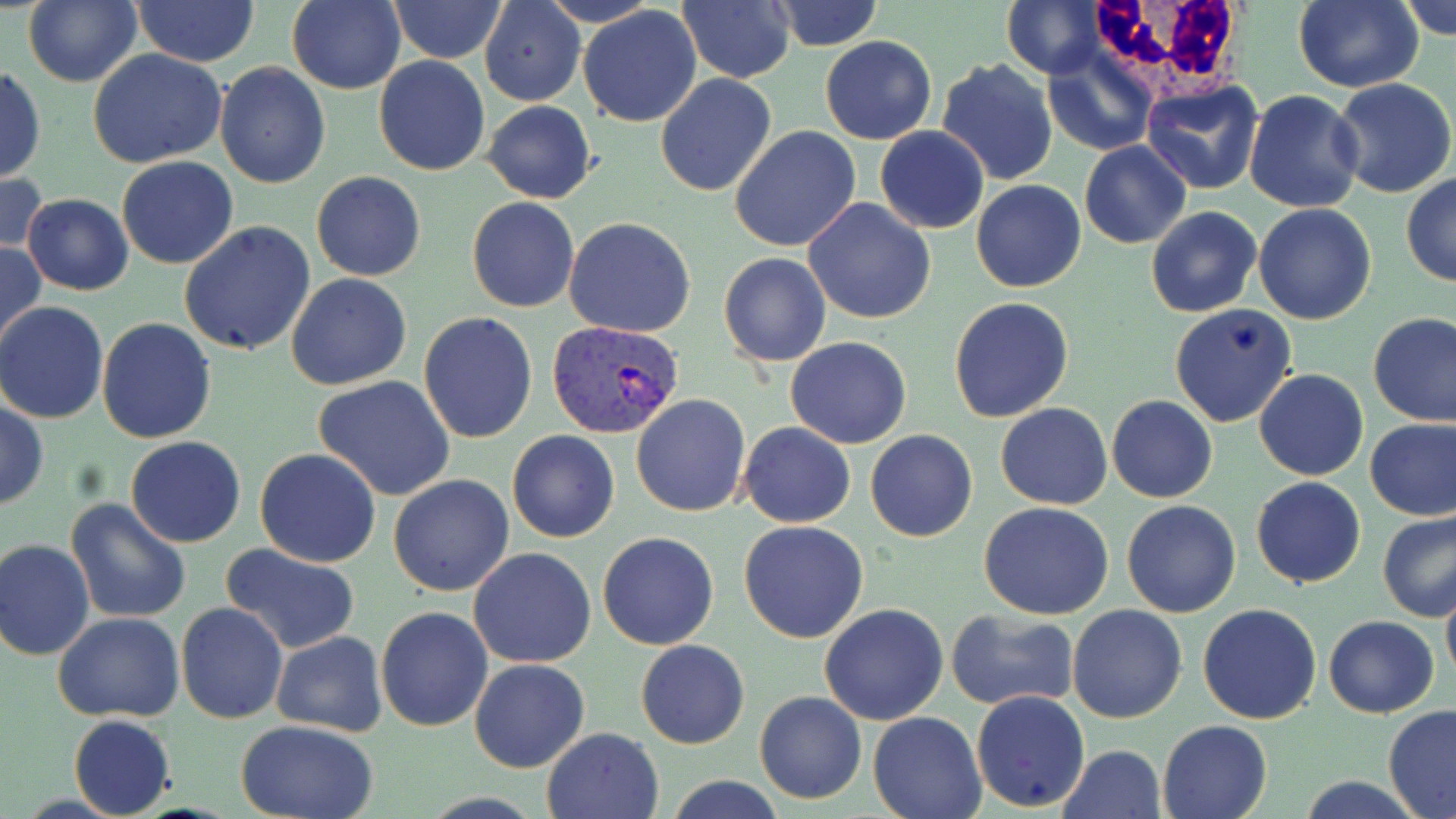
{
  "slide_level_diagnosis": "Plasmodium vivax",
  "field_of_view": "single",
  "white_blood_cell_locations": "approximate bounding boxes as named x1/y1/x2/y2 corners in pixels: (x1=1089, y1=0, x2=1248, y2=102)",
  "modality": "light microscopy",
  "plasmodium_vivax_infected_red_blood_cell_locations": "approximate bounding boxes as named x1/y1/x2/y2 corners in pixels: (x1=547, y1=320, x2=684, y2=439)",
  "stain": "May-Grünwald-Giemsa",
  "uninfected_red_blood_cell_locations": "approximate bounding boxes as named x1/y1/x2/y2 corners in pixels: (x1=23, y1=0, x2=142, y2=88), (x1=285, y1=0, x2=406, y2=93), (x1=537, y1=0, x2=661, y2=27), (x1=767, y1=0, x2=886, y2=51), (x1=1002, y1=0, x2=1105, y2=77), (x1=1293, y1=0, x2=1422, y2=93), (x1=1400, y1=0, x2=1456, y2=39), (x1=132, y1=1, x2=261, y2=67), (x1=390, y1=1, x2=506, y2=64), (x1=678, y1=1, x2=794, y2=83), (x1=480, y1=2, x2=584, y2=107), (x1=578, y1=5, x2=703, y2=129), (x1=820, y1=35, x2=936, y2=145), (x1=1044, y1=48, x2=1158, y2=156), (x1=87, y1=50, x2=228, y2=169), (x1=374, y1=55, x2=490, y2=176), (x1=937, y1=58, x2=1058, y2=186), (x1=213, y1=62, x2=332, y2=189), (x1=0, y1=66, x2=45, y2=184), (x1=655, y1=74, x2=778, y2=196), (x1=1141, y1=78, x2=1264, y2=195), (x1=1331, y1=78, x2=1456, y2=200), (x1=1244, y1=89, x2=1364, y2=212), (x1=482, y1=100, x2=597, y2=203), (x1=729, y1=125, x2=861, y2=252), (x1=874, y1=125, x2=989, y2=233), (x1=1079, y1=141, x2=1192, y2=250), (x1=116, y1=157, x2=240, y2=270), (x1=0, y1=169, x2=47, y2=264), (x1=311, y1=172, x2=426, y2=281), (x1=1401, y1=174, x2=1456, y2=286), (x1=970, y1=179, x2=1086, y2=293), (x1=22, y1=193, x2=132, y2=295), (x1=467, y1=197, x2=579, y2=313), (x1=804, y1=197, x2=936, y2=324), (x1=1253, y1=202, x2=1377, y2=324), (x1=1145, y1=205, x2=1262, y2=317), (x1=564, y1=217, x2=696, y2=337), (x1=178, y1=221, x2=316, y2=357), (x1=0, y1=238, x2=46, y2=350), (x1=717, y1=252, x2=832, y2=367), (x1=286, y1=273, x2=412, y2=390), (x1=949, y1=298, x2=1075, y2=422), (x1=0, y1=302, x2=111, y2=422), (x1=1169, y1=303, x2=1299, y2=429), (x1=419, y1=312, x2=539, y2=444), (x1=1369, y1=312, x2=1456, y2=426), (x1=96, y1=317, x2=217, y2=444), (x1=785, y1=336, x2=912, y2=449), (x1=1254, y1=367, x2=1369, y2=482), (x1=314, y1=376, x2=457, y2=501), (x1=630, y1=394, x2=751, y2=517), (x1=1107, y1=395, x2=1217, y2=504), (x1=0, y1=399, x2=48, y2=511), (x1=995, y1=403, x2=1112, y2=509), (x1=1365, y1=416, x2=1456, y2=522), (x1=738, y1=422, x2=855, y2=528), (x1=507, y1=430, x2=619, y2=543), (x1=864, y1=430, x2=978, y2=543), (x1=125, y1=437, x2=247, y2=548), (x1=255, y1=447, x2=382, y2=568), (x1=388, y1=474, x2=515, y2=597), (x1=1250, y1=477, x2=1366, y2=588), (x1=65, y1=497, x2=193, y2=623), (x1=1121, y1=499, x2=1241, y2=618), (x1=979, y1=501, x2=1114, y2=620), (x1=1378, y1=512, x2=1456, y2=623), (x1=738, y1=519, x2=870, y2=644), (x1=596, y1=530, x2=720, y2=651), (x1=0, y1=538, x2=95, y2=659), (x1=219, y1=543, x2=364, y2=656), (x1=468, y1=548, x2=597, y2=668), (x1=1441, y1=580, x2=1456, y2=687), (x1=175, y1=602, x2=288, y2=725), (x1=1197, y1=602, x2=1322, y2=724), (x1=818, y1=604, x2=949, y2=725), (x1=1068, y1=604, x2=1188, y2=723), (x1=375, y1=606, x2=494, y2=731), (x1=945, y1=609, x2=1078, y2=710), (x1=53, y1=612, x2=185, y2=723), (x1=1323, y1=614, x2=1440, y2=718), (x1=271, y1=630, x2=387, y2=738), (x1=636, y1=640, x2=749, y2=749), (x1=468, y1=658, x2=591, y2=773), (x1=754, y1=691, x2=866, y2=804), (x1=971, y1=691, x2=1090, y2=810), (x1=1383, y1=704, x2=1456, y2=817), (x1=868, y1=712, x2=986, y2=819), (x1=68, y1=715, x2=176, y2=818), (x1=1157, y1=718, x2=1274, y2=819), (x1=236, y1=719, x2=381, y2=819), (x1=541, y1=727, x2=663, y2=819), (x1=1056, y1=744, x2=1165, y2=819), (x1=660, y1=777, x2=790, y2=819), (x1=1295, y1=777, x2=1430, y2=817)",
  "preparation": "thin blood smear",
  "image_size": "1456×819 pixels",
  "magnification": "1000x"
}